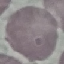
Summary:
  - Malaria status: uninfected
  - Image type: cell patch, automatically extracted from a larger field of view and resized to 64 × 64 pixels
  - Capture: smartphone camera at the microscope eyepiece
  - Preparation: thin blood film
  - Stain: Giemsa